State which parasite is depicted.
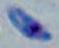
Toxoplasma gondii.

Photomicrograph. 1000x magnification.